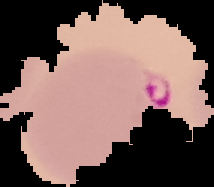
From a thin blood film. Image is 214×187 pixels. Segmented cell region on a black background. Result: malaria parasites identified.